Classify this cell by malaria status.
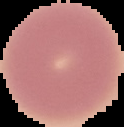

Uninfected.

Summary:
  - Preparation: thin blood smear
  - Image size: 124×127 pixels
  - Image type: segmented cell region with the area outside set to black